Identify the blood parasite species.
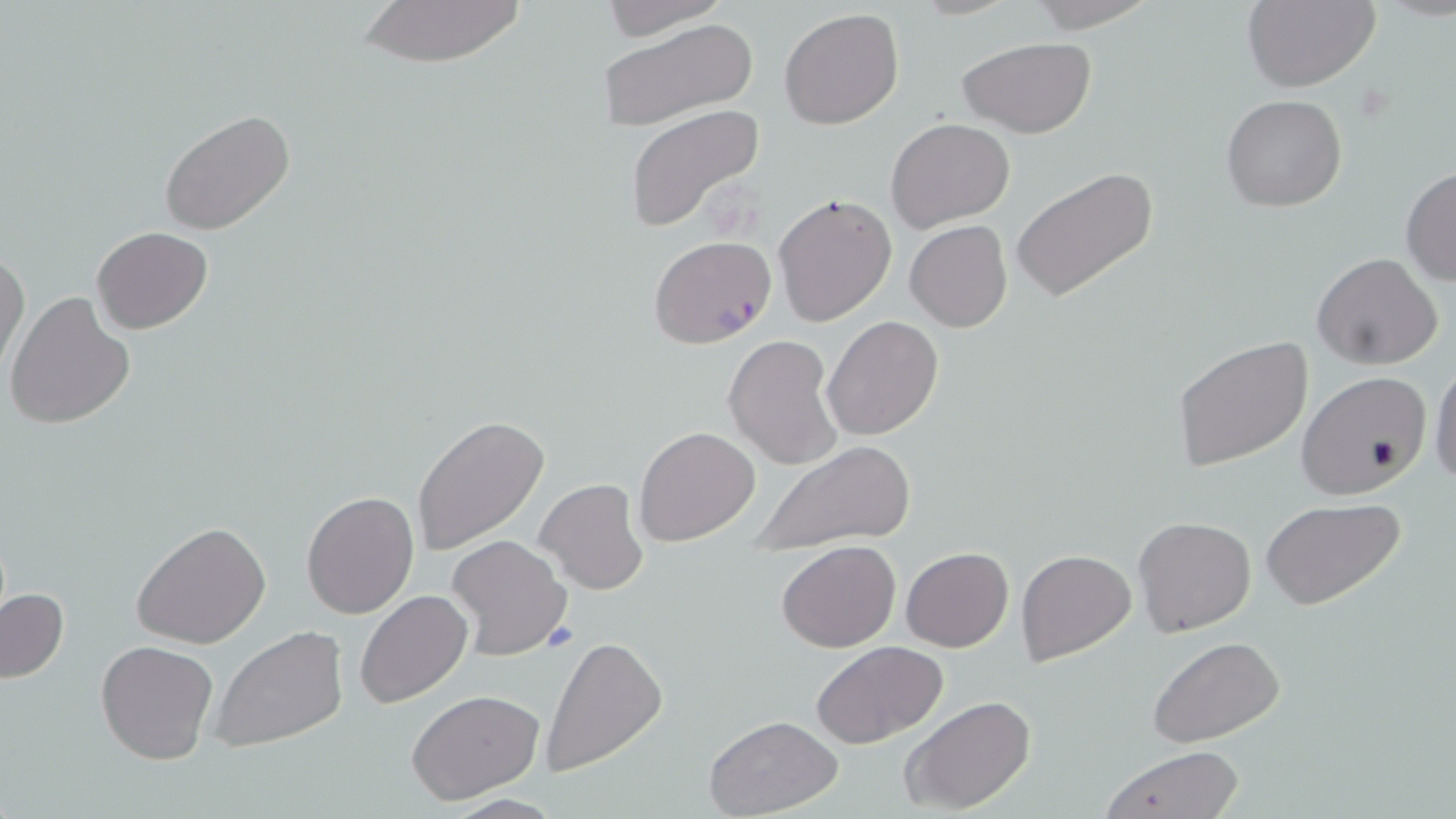

Plasmodium falciparum.

image_size: 1456×819 pixels
plasmodium_falciparum_infected_red_blood_cell_locations: 'approximate bounding boxes as named x1/y1/x2/y2 corners in pixels: (x1=649, y1=236, x2=777, y2=349)'
preparation: thin blood smear
modality: optical microscopy
uninfected_red_blood_cell_locations: 'approximate bounding boxes as named x1/y1/x2/y2 corners in pixels: (x1=349, y1=0, x2=530, y2=67), (x1=600, y1=0, x2=730, y2=40), (x1=1022, y1=0, x2=1161, y2=32), (x1=1242, y1=0, x2=1379, y2=91), (x1=779, y1=7, x2=905, y2=130), (x1=595, y1=17, x2=759, y2=135), (x1=957, y1=36, x2=1098, y2=138), (x1=1221, y1=94, x2=1348, y2=211), (x1=624, y1=104, x2=766, y2=232), (x1=159, y1=108, x2=295, y2=235), (x1=884, y1=118, x2=1015, y2=233), (x1=1400, y1=165, x2=1456, y2=288), (x1=1012, y1=167, x2=1158, y2=302), (x1=771, y1=191, x2=897, y2=328), (x1=904, y1=221, x2=1013, y2=332), (x1=91, y1=227, x2=213, y2=333), (x1=0, y1=248, x2=29, y2=376), (x1=1311, y1=251, x2=1443, y2=369), (x1=4, y1=290, x2=135, y2=431), (x1=823, y1=316, x2=944, y2=440), (x1=724, y1=334, x2=843, y2=473), (x1=1171, y1=335, x2=1315, y2=473), (x1=1429, y1=357, x2=1456, y2=491), (x1=1296, y1=370, x2=1433, y2=500), (x1=412, y1=416, x2=551, y2=555), (x1=634, y1=425, x2=761, y2=547), (x1=748, y1=439, x2=918, y2=554), (x1=534, y1=478, x2=649, y2=597), (x1=300, y1=490, x2=419, y2=619), (x1=1260, y1=498, x2=1406, y2=610), (x1=1132, y1=516, x2=1257, y2=636), (x1=132, y1=521, x2=272, y2=649), (x1=445, y1=534, x2=573, y2=661), (x1=777, y1=539, x2=901, y2=652), (x1=900, y1=546, x2=1013, y2=651), (x1=1016, y1=549, x2=1137, y2=666), (x1=1, y1=586, x2=70, y2=686), (x1=354, y1=591, x2=473, y2=709), (x1=208, y1=626, x2=351, y2=753), (x1=542, y1=635, x2=668, y2=776), (x1=1149, y1=638, x2=1286, y2=750), (x1=95, y1=639, x2=219, y2=766), (x1=810, y1=640, x2=949, y2=749), (x1=406, y1=689, x2=546, y2=806), (x1=900, y1=695, x2=1037, y2=815), (x1=704, y1=714, x2=843, y2=817), (x1=1097, y1=745, x2=1245, y2=819)'
magnification: 1000x
stain: May-Grünwald-Giemsa
field_of_view: one of a larger specimen